Locate Plasmodium parasites and leukocytes.
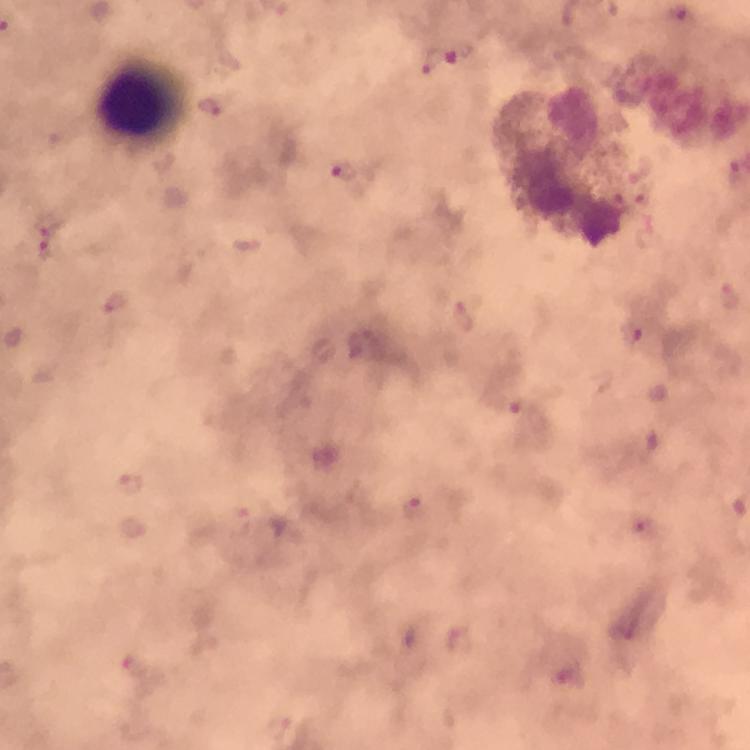
Approximate object centers, in pixels from the top-left corner.
Plasmodium parasites: (x=444, y=61), (x=344, y=170), (x=47, y=239), (x=633, y=332), (x=131, y=483), (x=416, y=508), (x=136, y=668), (x=568, y=674).
Leukocytes: (x=142, y=102).

Summary:
  - Stain: Giemsa
  - Image size: 750×750 pixels
  - Context: from a malaria diagnostic workup
  - Magnification: 100x
  - Preparation: thick blood smear
  - Immersion oil: used
  - Cropped from: one field of view
  - Capture: smartphone camera through the microscope